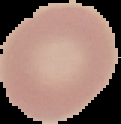

Summary:
  - Image type: segmented cell region on a black background
  - Preparation: thin blood film
  - Result: no malaria parasites detected
  - Image size: 121×124 pixels